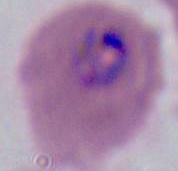

Summary:
  - Identification: Plasmodium
  - Magnification: 400x or 1000x
  - Modality: micrograph